Locate every leukocyte (white blood cell).
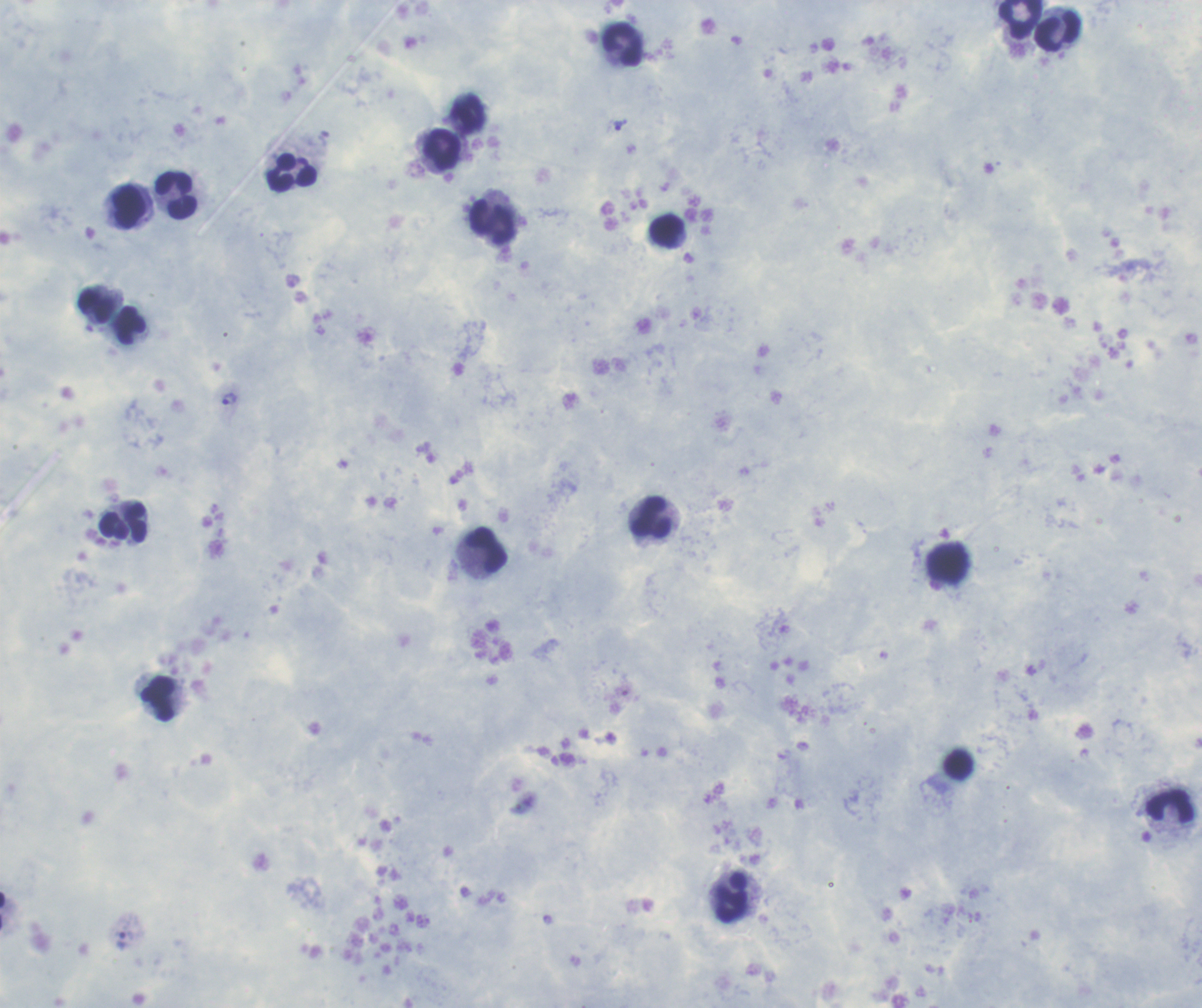

Approximate centers as {x, y} in pixels.
Leukocytes: {1019, 20}, {1057, 31}, {624, 45}, {467, 115}, {442, 149}, {292, 171}, {177, 195}, {129, 208}, {493, 221}, {666, 231}, {96, 306}, {130, 325}, {650, 519}, {123, 523}, {486, 550}, {947, 563}, {158, 699}, {1170, 807}, {733, 898}.

Approximate centers as {x, y} in pixels.
Summary:
  - Trophozoite locations: {620, 125}, {230, 399}, {126, 939}
  - Context: previously used in an actual diagnosis
  - Magnification: 100x
  - Background quality: satisfactory
  - Preparation: thick blood film
  - Image size: 1202×1008 pixels
  - Field of view: one from this slide
  - Coloration quality: good
  - Stain: Romanowsky
  - Result: positive for Plasmodium parasites